Give the extent of all Plasmodium falciparum-infected red blood cells.
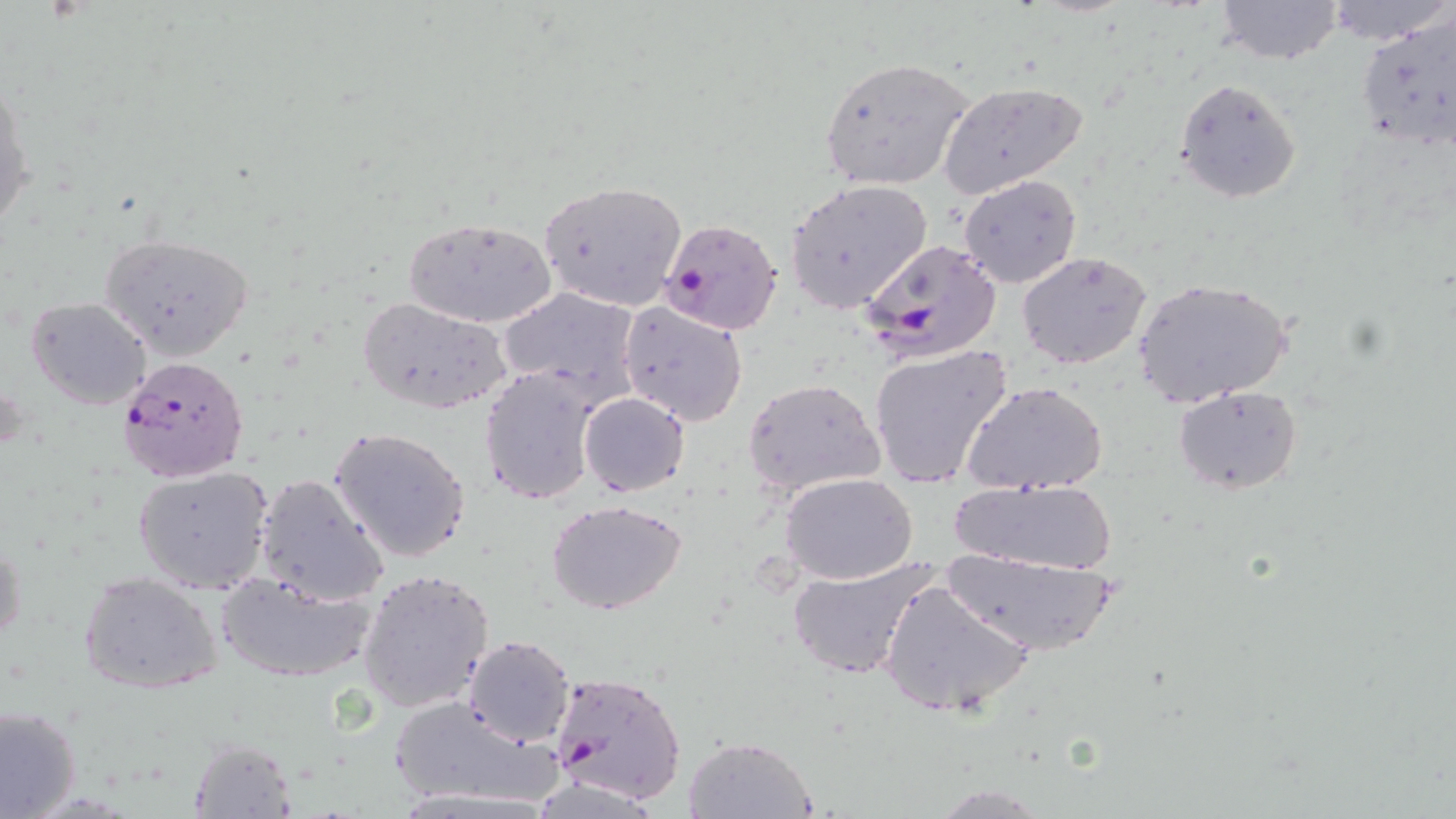
Approximate bounding boxes as named x1/y1/x2/y2 corners in pixels.
Plasmodium falciparum-infected red blood cells: (x1=658, y1=216, x2=784, y2=334), (x1=860, y1=238, x2=1003, y2=364), (x1=115, y1=355, x2=249, y2=483), (x1=550, y1=670, x2=687, y2=804).

Summary:
  - Uninfected red blood cell locations: (x1=1212, y1=0, x2=1345, y2=66), (x1=1355, y1=13, x2=1456, y2=153), (x1=818, y1=58, x2=976, y2=192), (x1=1, y1=76, x2=33, y2=239), (x1=1174, y1=77, x2=1302, y2=204), (x1=937, y1=81, x2=1088, y2=198), (x1=960, y1=174, x2=1081, y2=287), (x1=537, y1=180, x2=687, y2=313), (x1=786, y1=180, x2=932, y2=313), (x1=401, y1=215, x2=558, y2=327), (x1=98, y1=233, x2=253, y2=359), (x1=1017, y1=251, x2=1151, y2=369), (x1=1131, y1=277, x2=1292, y2=407), (x1=497, y1=286, x2=642, y2=408), (x1=28, y1=298, x2=151, y2=410), (x1=358, y1=298, x2=513, y2=415), (x1=619, y1=302, x2=749, y2=426), (x1=868, y1=344, x2=1016, y2=492), (x1=478, y1=365, x2=600, y2=505), (x1=744, y1=379, x2=884, y2=496), (x1=965, y1=382, x2=1107, y2=497), (x1=1173, y1=385, x2=1302, y2=496), (x1=578, y1=393, x2=689, y2=496), (x1=329, y1=426, x2=473, y2=563), (x1=132, y1=466, x2=275, y2=594), (x1=253, y1=472, x2=390, y2=606), (x1=781, y1=474, x2=916, y2=584), (x1=946, y1=477, x2=1125, y2=575), (x1=546, y1=499, x2=690, y2=616), (x1=1, y1=535, x2=23, y2=655), (x1=940, y1=551, x2=1124, y2=657), (x1=786, y1=553, x2=941, y2=682), (x1=357, y1=567, x2=495, y2=712), (x1=216, y1=569, x2=379, y2=682), (x1=77, y1=570, x2=224, y2=696), (x1=879, y1=579, x2=1033, y2=719), (x1=461, y1=635, x2=576, y2=745), (x1=385, y1=694, x2=561, y2=811), (x1=0, y1=704, x2=81, y2=818), (x1=682, y1=735, x2=817, y2=818), (x1=186, y1=738, x2=297, y2=816)
  - Slide-level diagnosis: Plasmodium falciparum
  - Image size: 1456×819 pixels
  - Stain: May-Grünwald-Giemsa
  - Preparation: thin blood smear
  - Field of view: single
  - Modality: optical microscopy
  - Magnification: 1000x